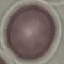

Summary:
  - Malaria status: uninfected
  - Stain: Giemsa
  - Capture: smartphone through the microscope eyepiece
  - Image type: cell patch, automatically extracted from a larger field of view and resized to 64 × 64 pixels
  - Preparation: thin smear